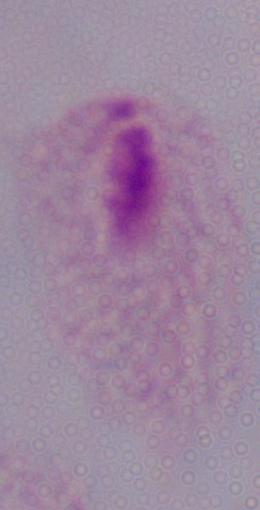

Summary:
  - Identification: trichomonad
  - Modality: micrograph
  - Magnification: 1000x